Point out every malaria parasite.
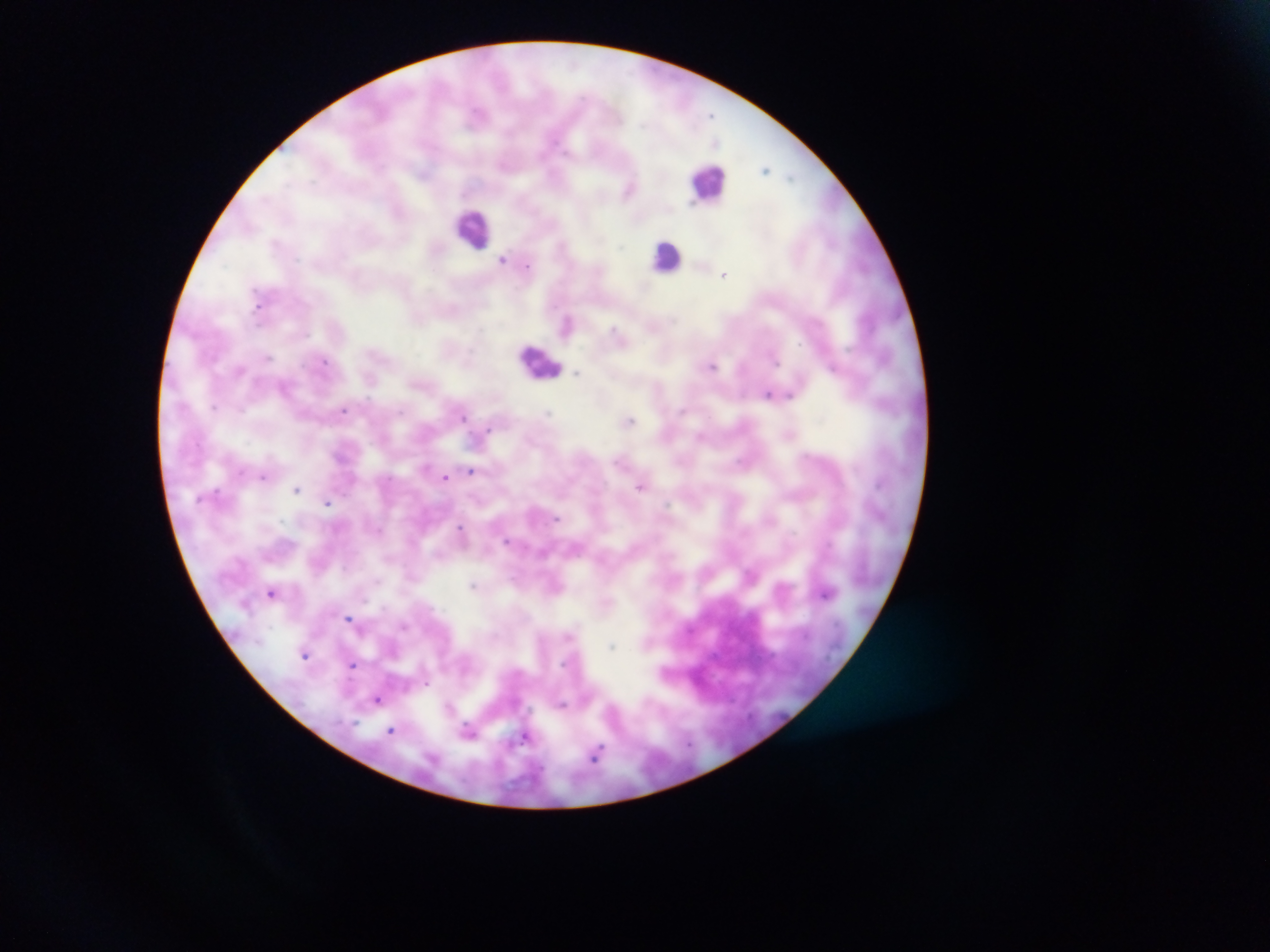

Approximate centers as {x, y} in pixels.
Malaria parasites: {765, 169}, {629, 189}, {503, 258}, {528, 265}, {724, 274}, {260, 304}, {568, 322}, {711, 366}, {577, 373}, {771, 394}, {344, 409}, {464, 416}, {630, 421}, {487, 431}, {470, 472}, {264, 477}, {446, 478}, {640, 485}, {297, 489}, {327, 501}, {462, 530}, {507, 541}, {474, 584}, {273, 592}, {349, 618}, {306, 653}, {352, 664}, {378, 699}, {391, 730}, {469, 730}, {526, 736}, {598, 752}.

preparation: thick blood smear
country: Ghana
capture: mobile-phone photograph through a microscope
field_of_view: single
leukocyte_locations: 'approximate centers as {x, y} in pixels: {708, 182}, {474, 228}, {667, 257}, {539, 362}'
image_size: 1270×952 pixels